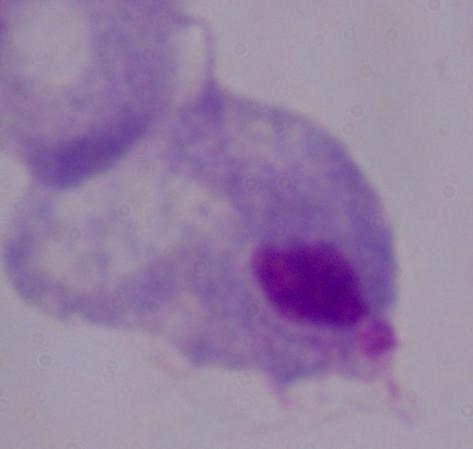
Captured at 1000x magnification. A trichomonad is seen. Micrograph.